Point out Plasmodium parasites and leukocytes.
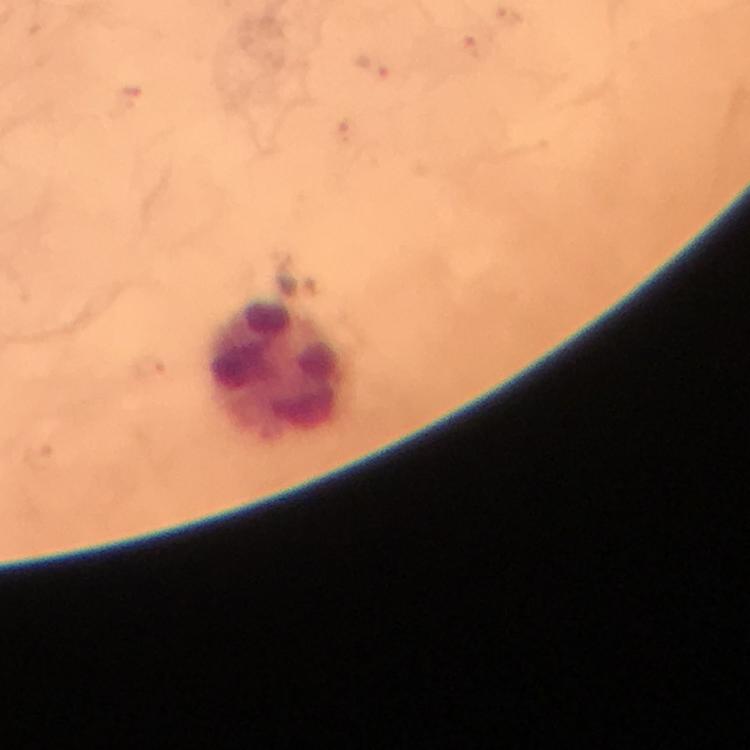

Approximate centers as {x, y} in pixels.
Plasmodium parasites: {372, 67}.
Leukocytes: {275, 372}.

Summary:
  - Preparation: thick blood smear
  - Stain: Giemsa
  - Cropped from: a single field of view
  - Magnification: 100x
  - Context: from a malaria diagnostic workup
  - Capture: smartphone photograph through a microscope
  - Immersion oil: used
  - Image size: 750×750 pixels